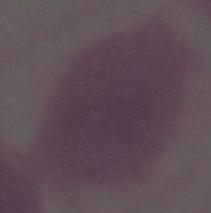

modality = micrograph
magnification = 1000x
identification = erythrocyte